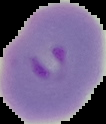

Result: Plasmodium parasites detected. The area outside the segmented cell region is set to black. From a thin blood film. Image is 106×124 pixels.